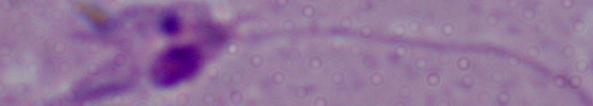
{
  "magnification": "1000x",
  "identification": "Leishmania",
  "modality": "photomicrograph"
}